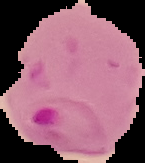

From a thin blood film. Result: Plasmodium parasites identified. Cell region segmented out of the field of view; the surrounding area is masked to black. Image is 145×163 pixels.